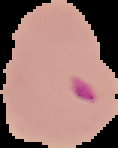
Summary:
  - Malaria status: parasitized
  - Image type: segmented cell region on a black background
  - Preparation: thin blood smear
  - Image size: 118×148 pixels